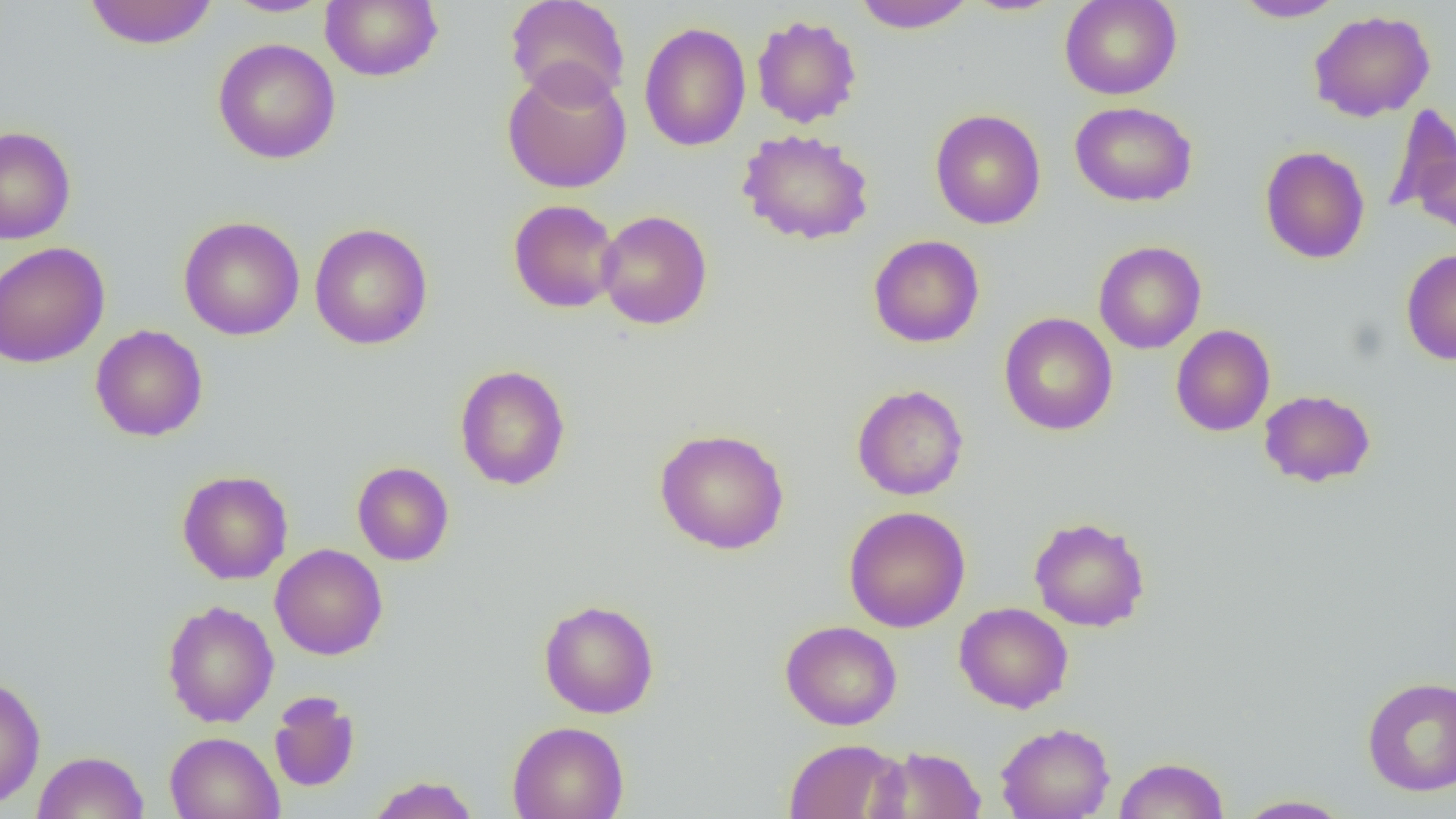

slide-level diagnosis = negative for blood parasites
preparation = thin blood smear
field of view = single
magnification = 1000x
modality = optical microscopy
uninfected red blood cell locations = approximate bounding boxes as (x1,y1)-(x2,y2) corner pairs in pixels: (82,0)-(219,50), (221,0)-(333,18), (321,0)-(443,82), (505,0)-(630,106), (851,0)-(977,32), (961,0)-(1067,17), (1059,0)-(1182,100), (1233,0)-(1347,22), (1308,10)-(1436,122), (751,14)-(863,128), (639,22)-(751,152), (212,38)-(341,164), (502,62)-(633,195), (1070,101)-(1198,207), (1384,104)-(1456,218), (930,109)-(1046,230), (0,126)-(76,244), (737,128)-(875,246), (1260,145)-(1370,264), (1412,148)-(1456,240), (508,199)-(622,313), (596,210)-(712,330), (178,216)-(305,341), (309,222)-(433,350), (868,234)-(985,348), (0,241)-(110,368), (1093,241)-(1206,354), (1401,247)-(1456,365), (998,312)-(1118,436), (90,324)-(209,442), (1171,324)-(1276,437), (455,364)-(571,491), (852,384)-(969,500), (1259,389)-(1376,488), (654,428)-(790,555), (352,461)-(454,566), (177,469)-(293,584), (843,506)-(971,633), (1029,515)-(1150,632), (270,543)-(388,660), (538,599)-(659,718), (162,600)-(279,728), (954,602)-(1074,714), (780,620)-(902,730), (0,674)-(46,810), (1362,676)-(1456,795), (268,691)-(361,792), (507,720)-(629,819), (995,722)-(1115,819), (165,731)-(284,819), (783,738)-(905,819), (870,745)-(987,819), (32,750)-(149,819), (1114,756)-(1229,818), (366,775)-(479,818), (1235,794)-(1355,818)
image size = 1456×819 pixels